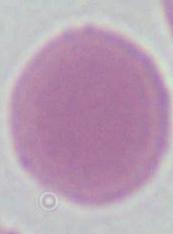

magnification: 1000x
identification: erythrocyte
modality: micrograph